Describe the morphology of the red blood cells.
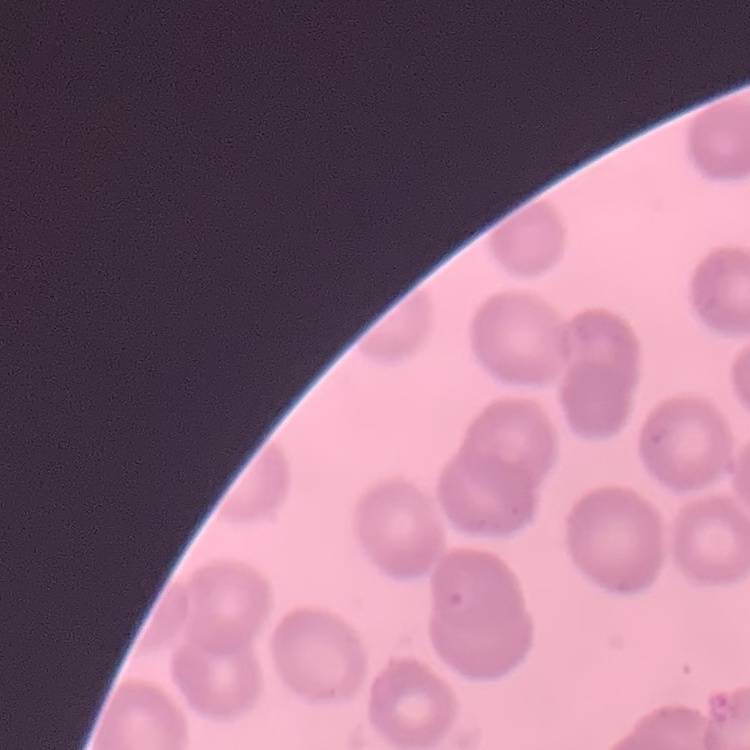

They show no rouleaux formation.

Summary:
  - Preparation: thin peripheral smear
  - Stain: Field's or Giemsa
  - Image type: square crop of a larger photomicrograph